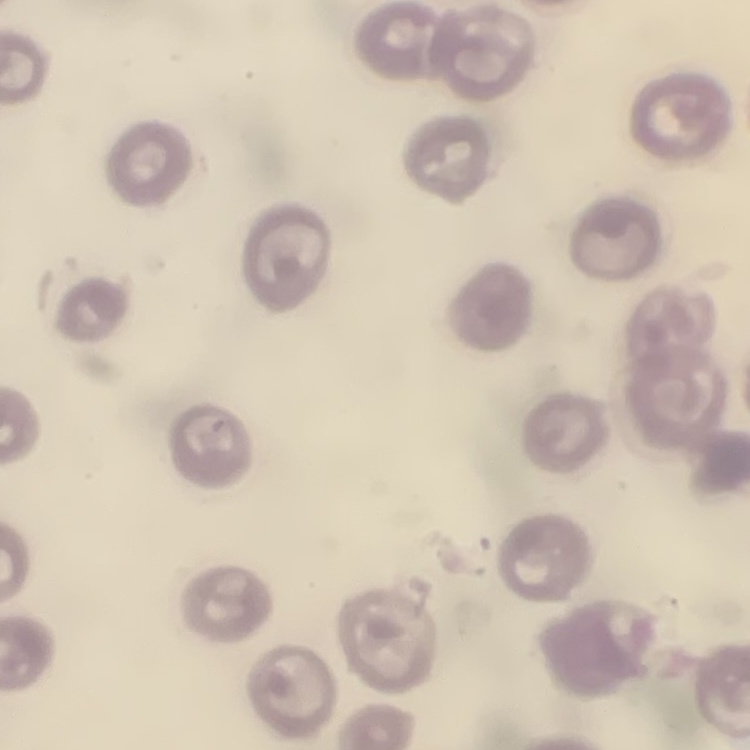

red_blood_cell_morphology: no rouleaux formation
preparation: thin peripheral smear
stain: Field's or Giemsa
image_type: square crop of a larger photomicrograph